Report the malaria status of this cell.
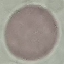
Uninfected.

Cell patch, automatically extracted from a larger field of view and resized to 64 × 64 pixels. Acquired by smartphone through the microscope eyepiece. Giemsa stain. Thin blood smear.